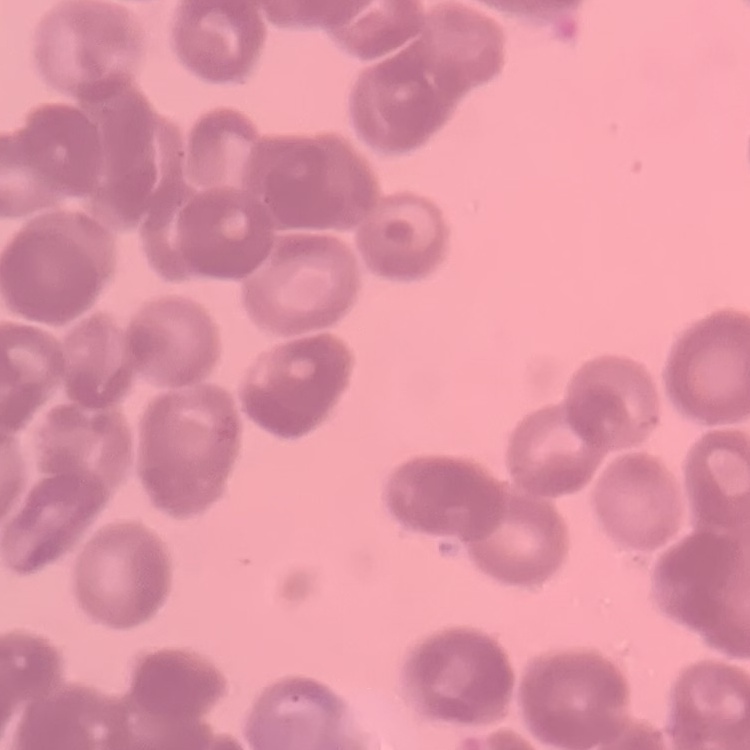
The red blood cells show rouleaux formation. Thin peripheral smear. Field's or Giemsa stain. One tile cut from a larger photomicrograph.